State the blood parasite species.
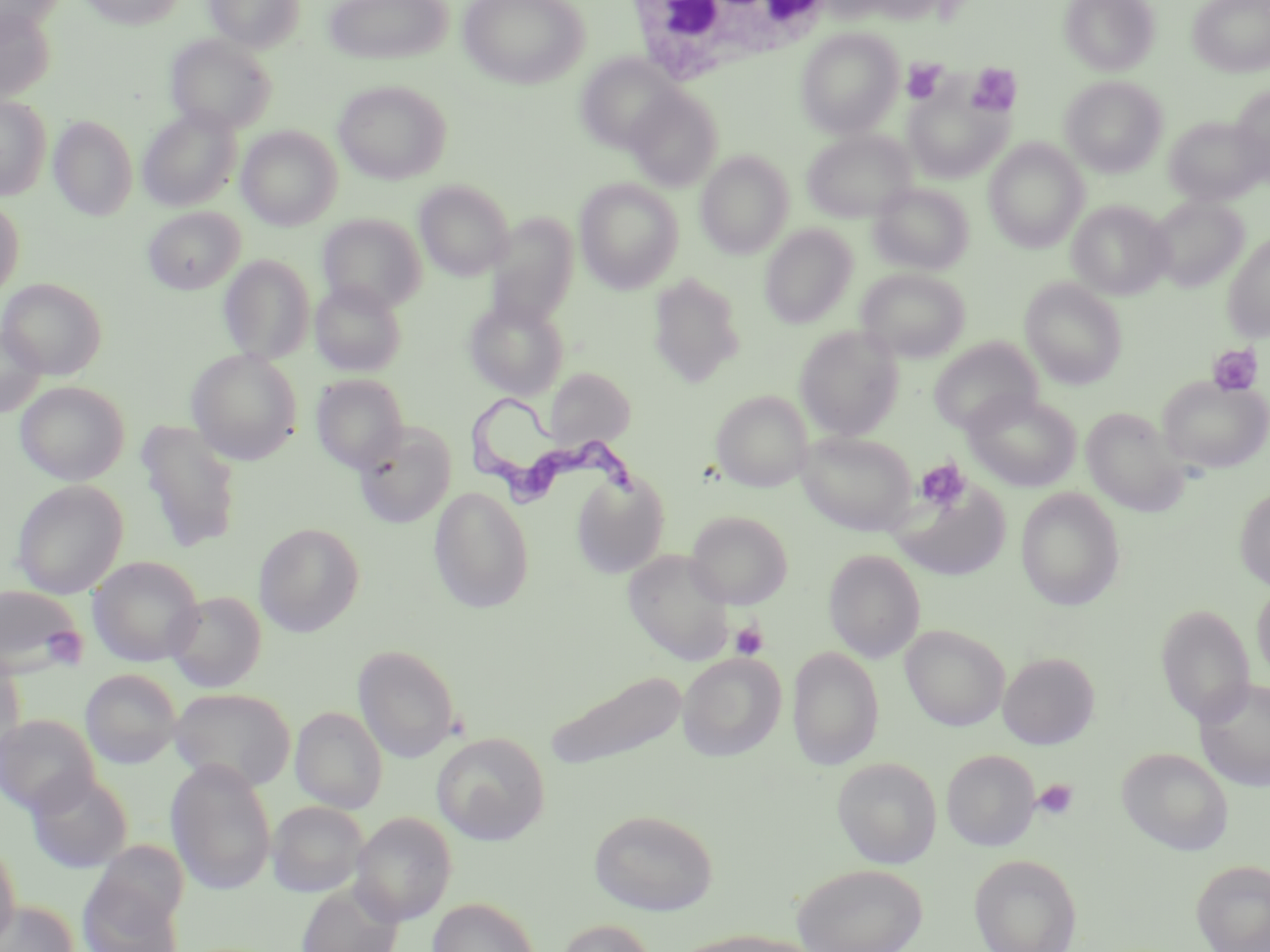

Trypanosoma brucei.

Summary:
  - Coordinate format: approximate bounding boxes as (x1, y1, x2, y2) in pixels
  - Trypanosoma brucei locations: (466, 396, 647, 510)
  - Uninfected red blood cell locations: (0, 0, 65, 35), (78, 0, 186, 29), (204, 0, 304, 52), (324, 0, 452, 65), (458, 0, 588, 89), (1060, 0, 1159, 75), (1189, 0, 1270, 77), (0, 5, 56, 102), (796, 27, 904, 138), (165, 34, 276, 134), (575, 53, 683, 154), (1061, 76, 1167, 176), (334, 79, 451, 185), (904, 82, 1013, 183), (1231, 85, 1270, 182), (625, 86, 724, 190), (0, 95, 51, 200), (138, 107, 240, 211), (49, 115, 138, 221), (1164, 115, 1267, 207), (236, 126, 342, 230), (802, 129, 916, 223), (984, 138, 1089, 252), (696, 151, 794, 259), (574, 177, 684, 293), (414, 180, 514, 280), (869, 183, 973, 275), (1148, 196, 1249, 292), (0, 198, 24, 298), (1068, 200, 1173, 299), (143, 207, 244, 294), (317, 213, 426, 312), (485, 214, 579, 326), (760, 224, 857, 328), (1222, 232, 1270, 342), (219, 254, 315, 364), (857, 268, 970, 362), (648, 273, 745, 387), (0, 277, 107, 378), (310, 279, 407, 376), (1021, 279, 1127, 388), (463, 296, 570, 400), (1, 322, 46, 417), (794, 325, 904, 440), (929, 338, 1043, 436), (187, 349, 302, 465), (545, 367, 636, 450), (311, 374, 409, 473), (1157, 375, 1270, 474), (16, 381, 130, 485), (711, 390, 813, 493), (963, 390, 1082, 492), (1081, 407, 1190, 516), (135, 420, 244, 553), (353, 422, 457, 529), (797, 429, 918, 535), (572, 471, 669, 578), (889, 477, 1012, 581), (12, 480, 128, 598), (428, 486, 535, 614), (1235, 486, 1270, 590), (1015, 487, 1126, 611), (686, 510, 792, 609), (254, 523, 364, 637), (623, 549, 736, 665), (824, 549, 925, 663), (88, 556, 204, 666), (1252, 581, 1270, 683), (0, 585, 87, 679), (166, 591, 266, 693), (1156, 604, 1254, 727), (900, 625, 1010, 731), (353, 644, 459, 763), (787, 647, 884, 771), (999, 651, 1100, 750), (0, 652, 25, 767), (678, 653, 785, 761), (81, 669, 181, 768), (544, 669, 688, 775), (1194, 677, 1270, 791), (169, 687, 295, 791), (290, 706, 387, 813), (0, 714, 100, 817), (432, 732, 550, 846), (1117, 747, 1233, 855), (942, 749, 1039, 851), (832, 757, 942, 868), (166, 760, 276, 894), (25, 770, 133, 873), (267, 801, 368, 897), (589, 809, 719, 915), (351, 812, 456, 925), (0, 840, 21, 946), (969, 853, 1082, 952), (80, 859, 186, 951), (1191, 859, 1270, 952), (792, 863, 928, 952), (294, 881, 404, 952), (427, 897, 539, 952), (1, 900, 80, 952), (554, 919, 658, 952), (677, 930, 823, 952)
  - Platelet locations: (902, 59, 946, 104), (966, 63, 1021, 117), (1207, 344, 1263, 396), (915, 458, 970, 512), (730, 620, 768, 660), (43, 626, 91, 669), (1032, 778, 1079, 821)
  - White blood cell locations: (624, 0, 841, 82)
  - Modality: light microscopy
  - Image size: 1270×952 pixels
  - Stain: May-Grünwald-Giemsa
  - Preparation: thin blood film
  - Field of view: one of a larger specimen
  - Magnification: 1000x